Locate every Plasmodium parasite.
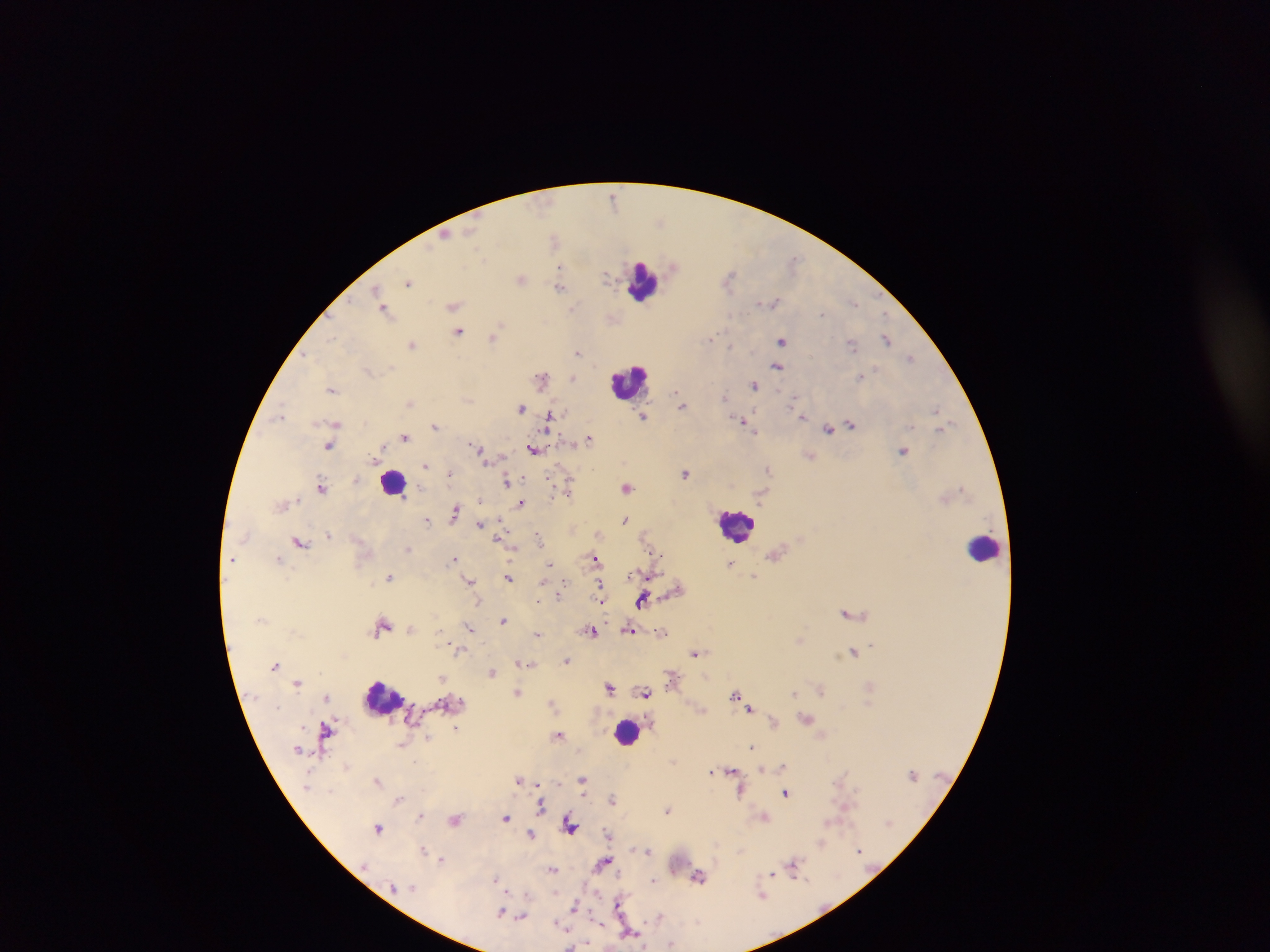

Approximate centers as (x, y) in pixels.
Plasmodium parasites: (613, 198), (444, 236), (554, 238), (674, 265), (560, 267), (607, 276), (730, 277), (522, 279), (409, 282), (560, 286), (376, 289), (379, 295), (853, 302), (772, 303), (453, 305), (383, 309), (822, 314), (458, 332), (331, 337), (493, 337), (711, 337), (886, 339), (782, 340), (412, 345), (852, 345), (730, 347), (578, 351), (307, 356), (912, 357), (777, 367), (861, 376), (542, 377), (573, 378), (755, 385), (332, 390), (678, 394), (725, 398), (794, 400), (409, 402), (682, 405), (520, 408), (936, 409), (798, 412), (280, 414), (643, 416), (550, 417), (802, 417), (742, 421), (336, 422), (852, 425), (435, 426), (944, 428), (828, 429), (754, 431), (405, 437), (588, 439), (330, 446), (477, 447), (534, 449), (903, 451), (426, 466), (769, 469), (685, 473), (450, 474), (506, 481), (569, 485), (322, 487), (627, 487), (962, 488), (521, 504), (454, 512), (427, 520), (625, 520), (479, 524), (329, 535), (539, 536), (497, 538), (300, 542), (407, 550), (657, 555), (279, 558), (454, 558), (232, 559), (595, 559), (549, 564), (730, 564), (754, 576), (390, 577), (508, 578), (470, 581), (599, 587), (559, 594), (601, 597), (643, 599), (850, 613), (503, 620), (382, 626), (470, 628), (411, 629), (630, 630), (591, 632), (662, 632), (537, 634), (872, 645), (459, 651), (853, 652), (696, 653), (566, 661), (522, 664), (275, 665), (492, 672), (442, 678), (297, 683), (610, 687), (821, 689), (517, 692), (794, 692), (646, 693), (734, 695), (327, 697), (552, 704), (749, 708), (806, 718), (774, 721), (456, 727), (326, 731), (559, 735), (429, 738), (401, 744), (752, 747), (783, 767), (761, 769), (732, 771), (712, 772), (519, 779), (583, 780), (378, 781), (539, 785), (740, 792), (786, 793), (612, 798), (398, 799), (541, 805), (668, 810), (421, 815), (763, 816), (506, 817), (455, 820), (829, 822), (570, 826), (378, 828), (531, 833), (607, 833), (821, 843), (423, 849), (649, 851), (859, 851), (441, 859), (604, 861), (794, 865), (553, 869), (772, 874), (698, 877), (495, 879), (653, 880), (526, 895), (762, 895), (620, 903), (574, 905), (501, 912), (659, 916), (521, 918), (559, 925), (629, 932), (672, 944).

Leukocyte locations: (642, 281), (628, 381), (393, 482), (736, 525), (985, 548), (381, 697), (626, 731). Sample from Ghana. Thick blood smear. Single field of view. Mobile-phone photograph taken through the microscope. Image is 1270×952 pixels.